Locate every blood parasite and identify its species.
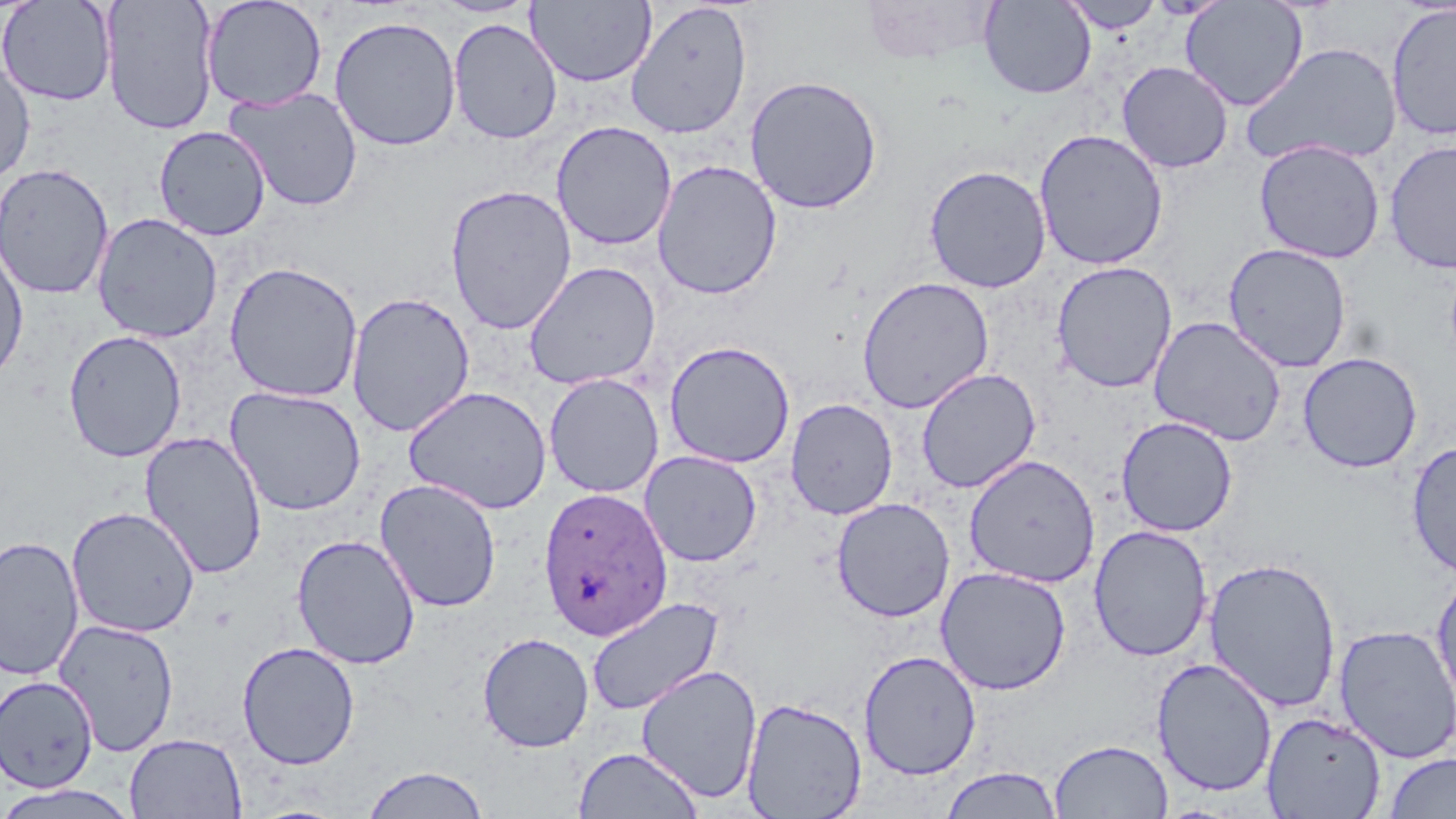
Approximate bounding boxes as [x1, y1, x2, y2] in pixels.
Plasmodium ovale-infected red blood cells: [538, 486, 672, 642].
No Plasmodium falciparum, Plasmodium malariae, Plasmodium vivax, Babesia divergens, or Trypanosoma brucei observed.

Summary:
  - Uninfected red blood cell locations: [0, 0, 117, 106], [101, 0, 220, 135], [201, 0, 328, 112], [429, 0, 540, 18], [527, 0, 656, 87], [979, 0, 1096, 98], [1060, 0, 1166, 33], [626, 1, 752, 140], [1180, 1, 1308, 111], [1386, 2, 1456, 142], [329, 15, 462, 151], [448, 17, 562, 144], [1241, 41, 1402, 169], [0, 58, 36, 185], [1117, 61, 1234, 173], [744, 75, 883, 214], [224, 86, 364, 212], [551, 121, 677, 251], [153, 125, 272, 241], [1033, 128, 1169, 270], [1254, 139, 1385, 264], [1384, 140, 1456, 274], [651, 159, 783, 300], [0, 162, 115, 301], [923, 164, 1052, 293], [444, 184, 578, 335], [92, 212, 223, 343], [0, 241, 29, 386], [1223, 242, 1352, 373], [223, 261, 364, 403], [524, 261, 661, 390], [1051, 261, 1178, 393], [856, 276, 994, 413], [346, 292, 476, 437], [1148, 315, 1288, 446], [63, 329, 187, 462], [663, 340, 796, 468], [1298, 352, 1423, 474], [915, 367, 1041, 494], [543, 373, 665, 498], [403, 385, 552, 515], [225, 386, 366, 516], [785, 397, 898, 519], [1116, 416, 1238, 537], [139, 431, 268, 580], [1405, 440, 1456, 578], [639, 450, 762, 567], [963, 454, 1100, 587], [374, 477, 502, 613], [830, 497, 956, 622], [66, 506, 200, 638], [1088, 525, 1213, 662], [292, 534, 421, 670], [0, 536, 84, 681], [1204, 557, 1342, 712], [935, 566, 1072, 695], [1431, 568, 1456, 712], [585, 596, 724, 716], [53, 618, 180, 756], [1333, 624, 1456, 763], [477, 632, 594, 753], [237, 641, 361, 769], [859, 650, 981, 780], [1151, 657, 1278, 798], [635, 664, 762, 802], [0, 675, 99, 793], [740, 696, 867, 819], [1260, 710, 1386, 818], [124, 733, 247, 818], [1049, 738, 1173, 818], [573, 746, 704, 819], [1384, 753, 1456, 818], [361, 765, 490, 818], [939, 766, 1064, 818], [0, 784, 141, 819]
  - Slide-level diagnosis: Plasmodium ovale
  - Field of view: one of a larger specimen
  - Image size: 1456×819 pixels
  - Preparation: thin blood film
  - Modality: light microscopy
  - Magnification: 1000x
  - Stain: May-Grünwald-Giemsa